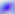

Summary:
  - Identification: Toxoplasma gondii
  - Modality: photomicrograph
  - Magnification: 400x